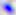
Summary:
  - Identification: Toxoplasma gondii
  - Modality: photomicrograph
  - Magnification: 400x